Identify the parasite.
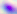
Toxoplasma gondii.

400x magnification. Micrograph.